Name the cell type shown.
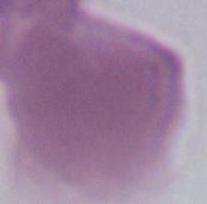
An erythrocyte.

modality = micrograph
magnification = 1000x